State the blood parasite species.
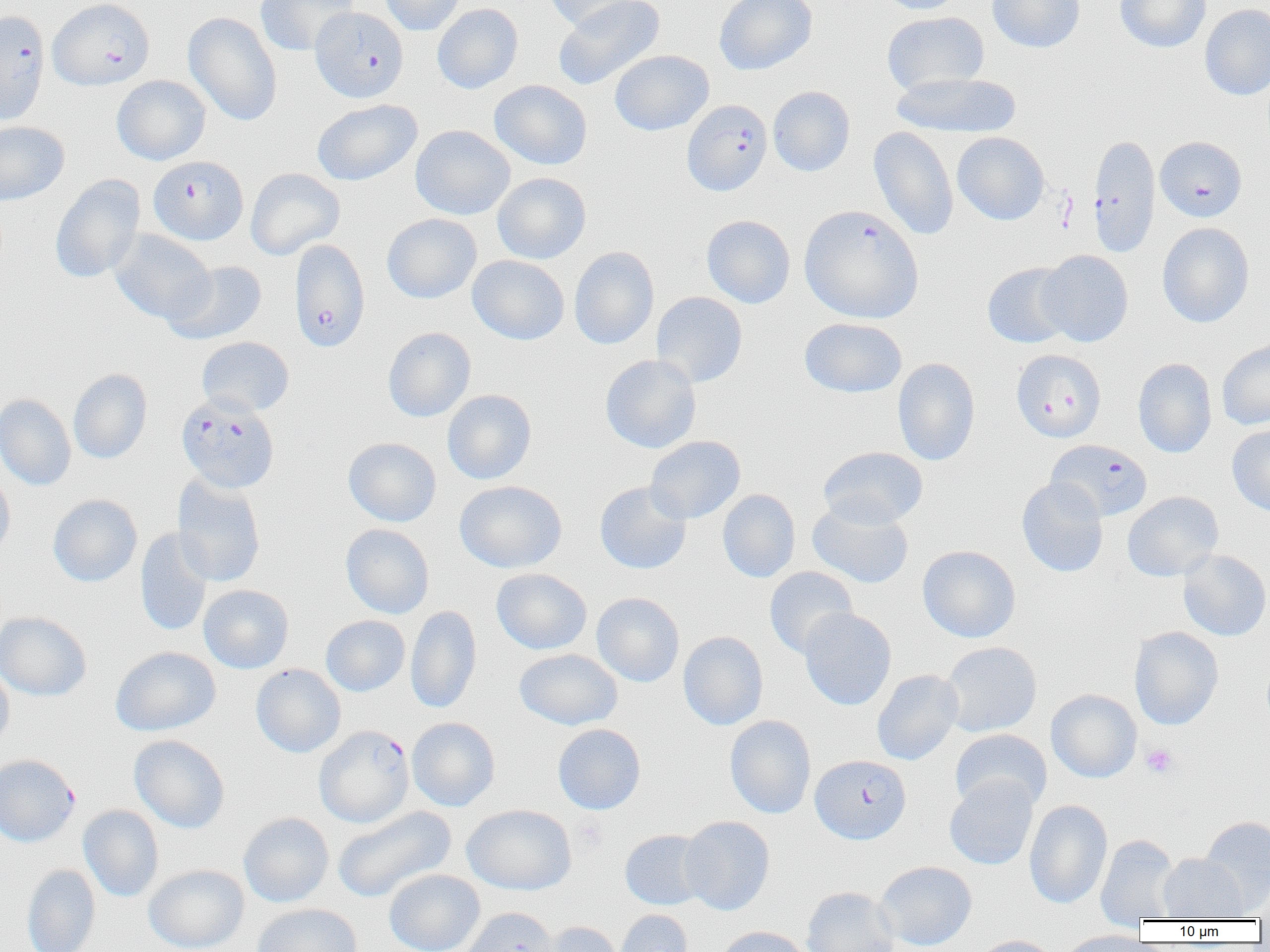
Plasmodium falciparum.

Summary:
  - Coordinate format: approximate bounding boxes as named x1/y1/x2/y2 corners in pixels
  - Uninfected red blood cell locations: (x1=255, y1=0, x2=359, y2=56), (x1=379, y1=0, x2=466, y2=35), (x1=543, y1=0, x2=644, y2=31), (x1=553, y1=0, x2=666, y2=90), (x1=714, y1=0, x2=817, y2=75), (x1=877, y1=0, x2=967, y2=14), (x1=987, y1=0, x2=1085, y2=53), (x1=1115, y1=0, x2=1211, y2=52), (x1=432, y1=3, x2=523, y2=94), (x1=1199, y1=3, x2=1270, y2=101), (x1=183, y1=12, x2=282, y2=126), (x1=881, y1=12, x2=989, y2=95), (x1=610, y1=49, x2=714, y2=135), (x1=891, y1=71, x2=1021, y2=139), (x1=112, y1=75, x2=210, y2=165), (x1=490, y1=80, x2=592, y2=170), (x1=768, y1=86, x2=855, y2=176), (x1=312, y1=99, x2=422, y2=186), (x1=0, y1=121, x2=69, y2=205), (x1=410, y1=125, x2=515, y2=220), (x1=868, y1=126, x2=958, y2=241), (x1=952, y1=132, x2=1049, y2=225), (x1=245, y1=168, x2=345, y2=259), (x1=492, y1=172, x2=591, y2=264), (x1=50, y1=174, x2=145, y2=283), (x1=382, y1=213, x2=481, y2=304), (x1=701, y1=215, x2=795, y2=308), (x1=1157, y1=222, x2=1254, y2=328), (x1=110, y1=229, x2=215, y2=324), (x1=569, y1=246, x2=659, y2=350), (x1=1038, y1=250, x2=1133, y2=347), (x1=467, y1=255, x2=569, y2=345), (x1=163, y1=261, x2=268, y2=345), (x1=982, y1=262, x2=1075, y2=349), (x1=651, y1=292, x2=748, y2=387), (x1=799, y1=317, x2=907, y2=398), (x1=383, y1=327, x2=476, y2=422), (x1=196, y1=336, x2=294, y2=416), (x1=1217, y1=338, x2=1270, y2=430), (x1=600, y1=354, x2=701, y2=454), (x1=893, y1=358, x2=980, y2=466), (x1=1133, y1=358, x2=1217, y2=458), (x1=68, y1=369, x2=152, y2=464), (x1=442, y1=389, x2=537, y2=484), (x1=0, y1=394, x2=76, y2=490), (x1=1227, y1=425, x2=1270, y2=515), (x1=645, y1=435, x2=745, y2=523), (x1=343, y1=437, x2=441, y2=526), (x1=817, y1=446, x2=928, y2=529), (x1=0, y1=469, x2=15, y2=561), (x1=172, y1=474, x2=266, y2=588), (x1=1017, y1=478, x2=1108, y2=577), (x1=454, y1=480, x2=567, y2=573), (x1=594, y1=481, x2=692, y2=574), (x1=718, y1=489, x2=801, y2=582), (x1=1122, y1=491, x2=1223, y2=581), (x1=48, y1=494, x2=142, y2=587), (x1=807, y1=501, x2=914, y2=589), (x1=341, y1=524, x2=434, y2=618), (x1=134, y1=528, x2=213, y2=636), (x1=917, y1=545, x2=1021, y2=643), (x1=1178, y1=549, x2=1270, y2=641), (x1=764, y1=567, x2=858, y2=659), (x1=491, y1=568, x2=592, y2=655), (x1=198, y1=584, x2=294, y2=673), (x1=591, y1=592, x2=685, y2=687), (x1=405, y1=605, x2=482, y2=713), (x1=799, y1=608, x2=897, y2=711), (x1=0, y1=611, x2=92, y2=701), (x1=321, y1=615, x2=410, y2=696), (x1=1129, y1=626, x2=1223, y2=730), (x1=678, y1=631, x2=768, y2=730), (x1=942, y1=642, x2=1042, y2=737), (x1=111, y1=646, x2=221, y2=736), (x1=514, y1=649, x2=623, y2=730), (x1=0, y1=664, x2=14, y2=753), (x1=251, y1=664, x2=346, y2=757), (x1=872, y1=669, x2=963, y2=765), (x1=1046, y1=689, x2=1142, y2=782), (x1=724, y1=715, x2=816, y2=818), (x1=407, y1=717, x2=500, y2=811), (x1=552, y1=723, x2=646, y2=814), (x1=950, y1=729, x2=1052, y2=813), (x1=129, y1=734, x2=230, y2=833), (x1=945, y1=775, x2=1038, y2=870), (x1=1024, y1=799, x2=1112, y2=909), (x1=462, y1=804, x2=577, y2=895), (x1=78, y1=805, x2=164, y2=902), (x1=332, y1=807, x2=456, y2=903), (x1=238, y1=812, x2=334, y2=907), (x1=679, y1=816, x2=775, y2=915), (x1=1199, y1=816, x2=1270, y2=914), (x1=620, y1=829, x2=711, y2=910), (x1=1095, y1=834, x2=1181, y2=925), (x1=1158, y1=853, x2=1247, y2=921), (x1=875, y1=861, x2=977, y2=951), (x1=22, y1=864, x2=101, y2=952), (x1=143, y1=864, x2=249, y2=952), (x1=384, y1=869, x2=485, y2=952), (x1=802, y1=887, x2=900, y2=952), (x1=251, y1=903, x2=362, y2=952), (x1=459, y1=906, x2=560, y2=952), (x1=615, y1=909, x2=693, y2=952), (x1=533, y1=921, x2=625, y2=952), (x1=715, y1=926, x2=811, y2=952), (x1=1059, y1=929, x2=1152, y2=952), (x1=972, y1=935, x2=1061, y2=952)
  - Platelet locations: (x1=1141, y1=744, x2=1178, y2=778), (x1=574, y1=816, x2=609, y2=854)
  - Plasmodium falciparum-infected red blood cell locations: (x1=48, y1=0, x2=155, y2=90), (x1=311, y1=7, x2=409, y2=103), (x1=0, y1=9, x2=49, y2=125), (x1=682, y1=99, x2=772, y2=196), (x1=1088, y1=134, x2=1160, y2=257), (x1=1155, y1=136, x2=1247, y2=222), (x1=148, y1=155, x2=248, y2=245), (x1=799, y1=204, x2=923, y2=324), (x1=289, y1=239, x2=370, y2=353), (x1=1011, y1=349, x2=1106, y2=442), (x1=176, y1=393, x2=279, y2=493), (x1=1046, y1=439, x2=1152, y2=521), (x1=314, y1=725, x2=414, y2=827), (x1=5, y1=752, x2=76, y2=845), (x1=810, y1=755, x2=911, y2=844)
  - Magnification: 1000x
  - Preparation: thin blood film
  - Modality: optical microscopy
  - Field of view: single
  - Image size: 1270×952 pixels